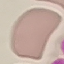
Summary:
  - Result: negative for malaria parasites
  - Capture: smartphone camera at the microscope eyepiece
  - Image type: cell patch, automatically extracted from a larger field of view and resized to 64 × 64 pixels
  - Preparation: thin blood smear
  - Stain: Giemsa